Classify this cell by malaria status.
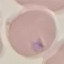

Parasitized.

image type = cell patch, automatically extracted from a larger field of view and resized to 64 × 64 pixels
preparation = thin blood smear
capture = smartphone camera at the microscope eyepiece
stain = Giemsa